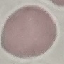

{
  "malaria_status": "uninfected",
  "preparation": "thin blood smear",
  "stain": "Giemsa",
  "image_type": "automatically extracted cell patch, resized to 64 × 64 pixels",
  "capture": "smartphone through the microscope eyepiece"
}